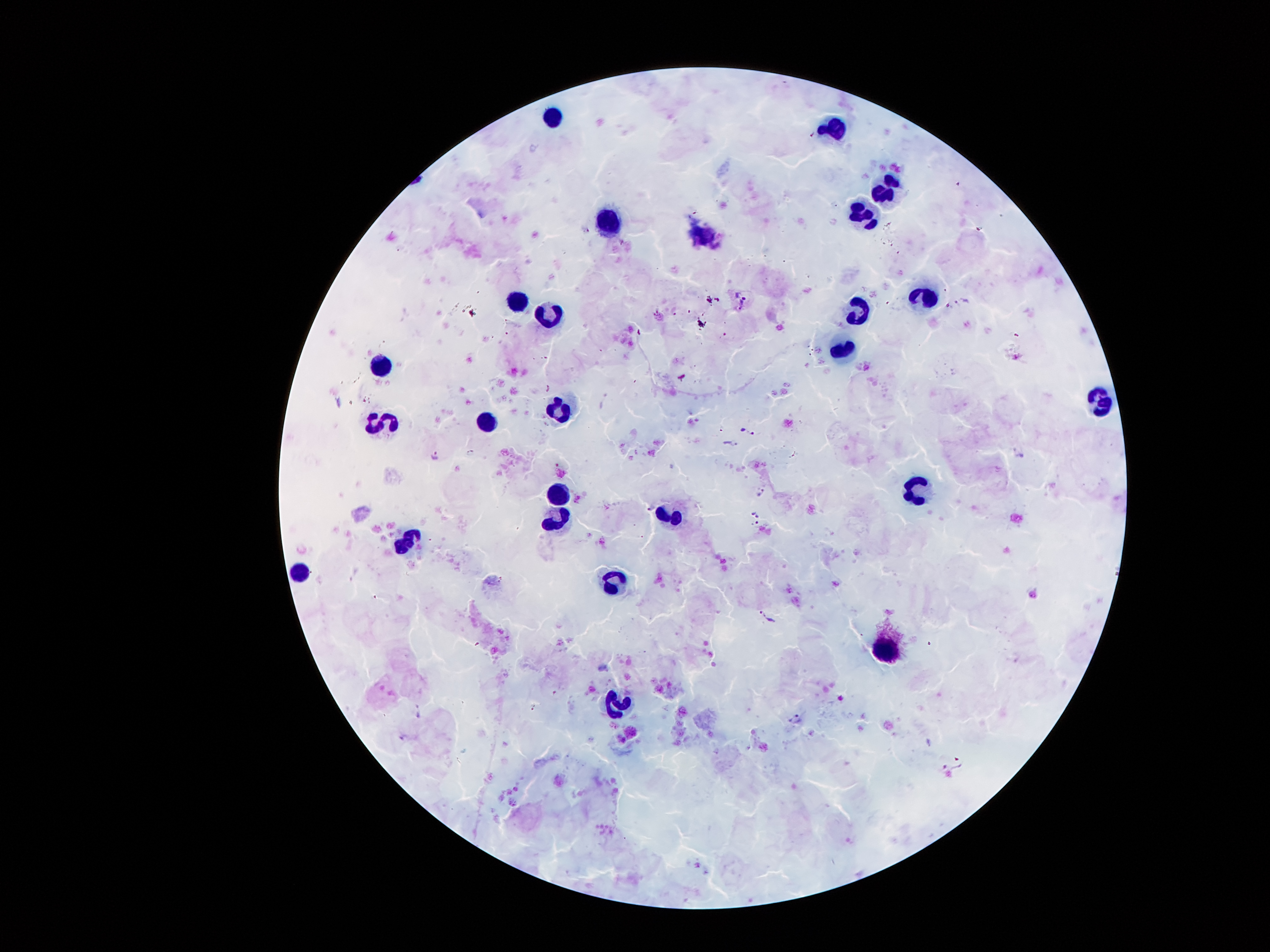
{
  "field_of_view": "one from this slide",
  "stain": "Giemsa",
  "leukocyte_locations": "approximate centers as {x, y} in pixels: {554, 117}, {837, 127}, {887, 186}, {864, 217}, {609, 224}, {926, 295}, {514, 301}, {859, 313}, {551, 315}, {842, 350}, {379, 364}, {1101, 397}, {561, 409}, {383, 417}, {488, 425}, {918, 489}, {561, 490}, {672, 515}, {561, 517}, {407, 542}, {297, 574}, {617, 580}, {889, 651}, {617, 701}",
  "capture": "smartphone camera through the microscope eyepiece",
  "preparation": "thick peripheral-blood smear",
  "patient_malaria_status": "infected with Plasmodium falciparum",
  "magnification": "100x",
  "image_size": "1270×952 pixels",
  "malaria_parasite_locations": "approximate centers as {x, y} in pixels: {435, 454}, {652, 508}, {756, 514}, {758, 525}, {403, 738}"
}